Describe the morphology of the erythrocytes.
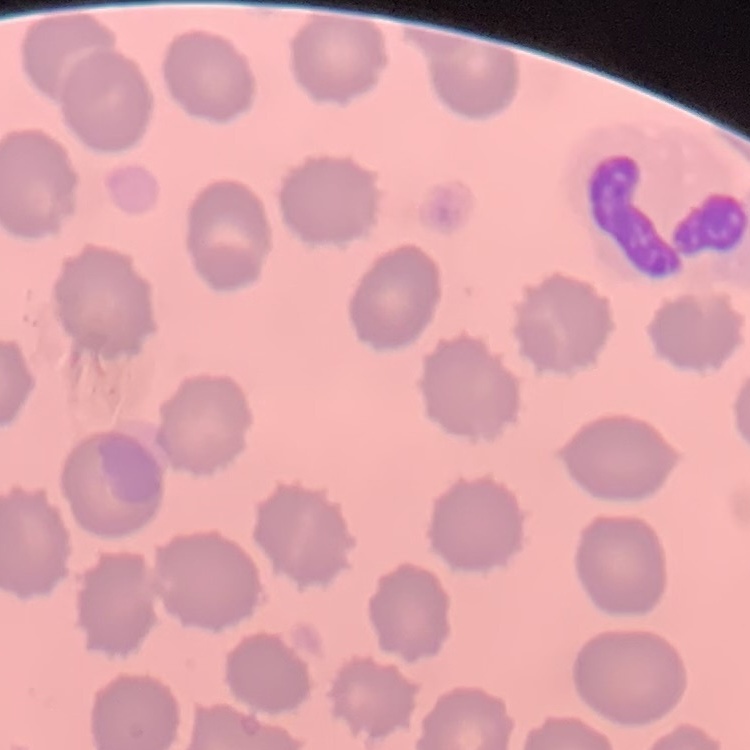

No rouleaux formation.

Summary:
  - Image type: one tile cut from a larger photomicrograph
  - Stain: Field's or Giemsa
  - Preparation: thin peripheral smear